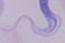

Summary:
  - Modality: micrograph
  - Identification: trypanosome
  - Magnification: 1000x